Report the malaria status of this cell.
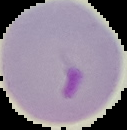
It is parasitized.

Summary:
  - Image size: 127×130 pixels
  - Image type: cell region segmented out of the field of view; surrounding area masked to black
  - Preparation: thin blood smear